Name the cell type shown.
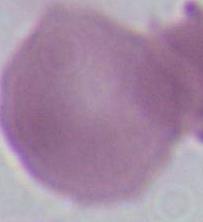

This is an erythrocyte.

Micrograph. Captured at 1000x magnification.